State the blood parasite species.
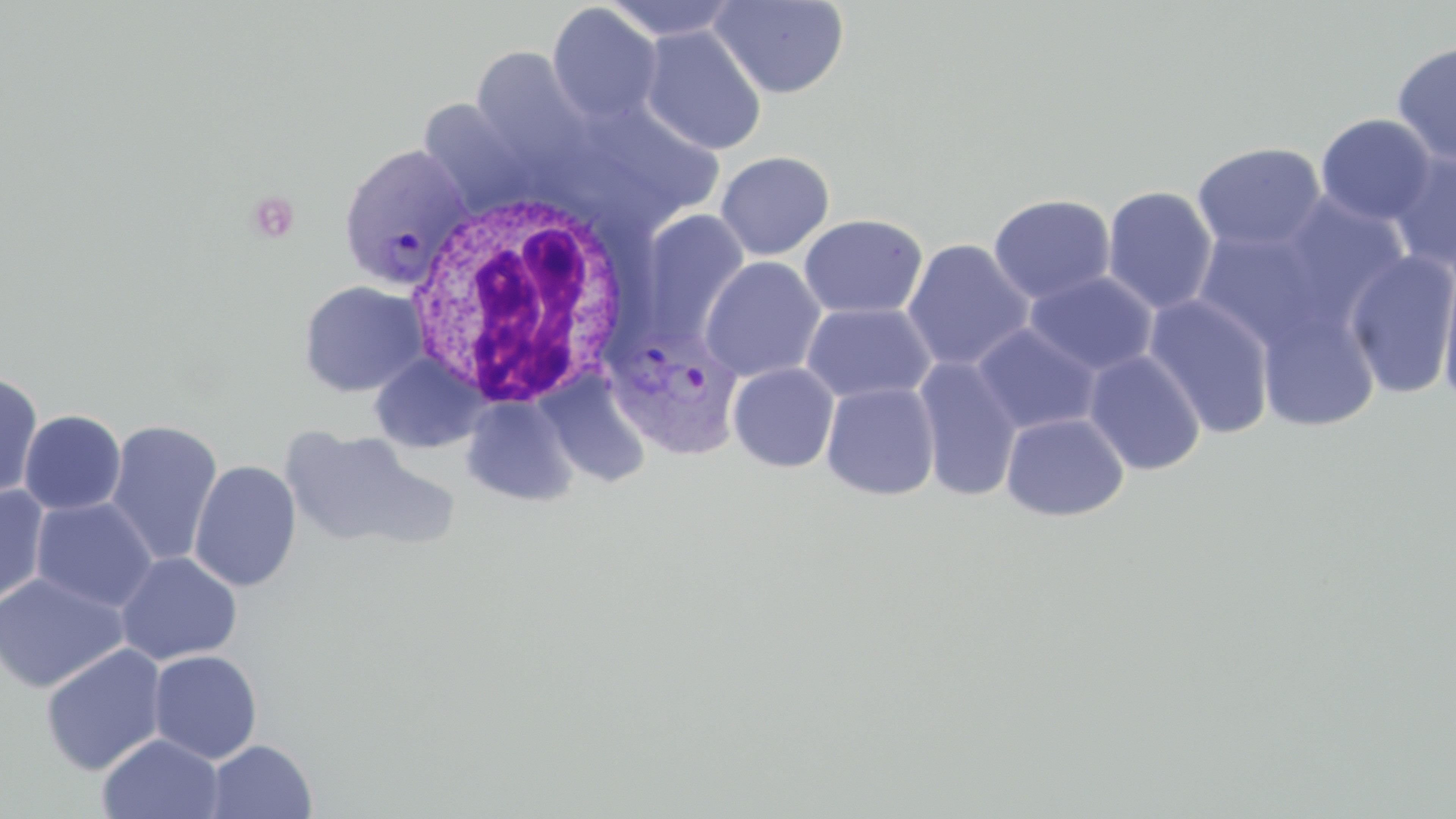
Plasmodium vivax.

Approximate bounding boxes as (x1,y1)-(x2,y2) corner pairs in pixels. Uninfected red blood cell locations: (601,0)-(742,42), (710,1)-(849,99), (547,4)-(663,124), (640,26)-(767,155), (1391,41)-(1456,166), (471,48)-(592,172), (556,95)-(728,230), (420,100)-(537,217), (1316,113)-(1436,226), (1192,141)-(1326,253), (1388,147)-(1456,275), (715,151)-(835,260), (1102,185)-(1219,314), (988,193)-(1116,305), (1266,193)-(1412,333), (636,209)-(750,344), (798,213)-(928,320), (1192,225)-(1333,351), (902,238)-(1035,372), (1344,249)-(1456,399), (1438,255)-(1456,410), (700,256)-(826,382), (1025,270)-(1158,375), (299,281)-(427,397), (1143,294)-(1277,439), (1255,301)-(1382,433), (801,302)-(937,404), (972,323)-(1101,435), (1083,350)-(1205,475), (370,353)-(487,454), (913,356)-(1024,502), (728,362)-(840,472), (0,370)-(43,503), (538,370)-(653,487), (820,381)-(941,500), (461,396)-(579,506), (18,409)-(126,515), (1000,411)-(1130,522), (104,419)-(223,566), (279,426)-(450,553), (188,460)-(302,592), (0,484)-(50,607), (31,497)-(158,612), (115,551)-(242,665), (0,572)-(129,693), (40,644)-(168,776), (148,650)-(263,764), (96,733)-(225,819), (204,739)-(318,818). Plasmodium vivax-infected red blood cell locations: (337,144)-(473,291), (605,323)-(742,460). White blood cell locations: (406,191)-(636,409). Image is 1456×819 pixels. Captured at 1000x magnification. May-Grünwald-Giemsa-stained preparation. Single field of view. Thin blood smear. Optical microscopy.